Find the red blood cells and label each as P. falciparum-infected, uninfected, or of indeterminate infection status.
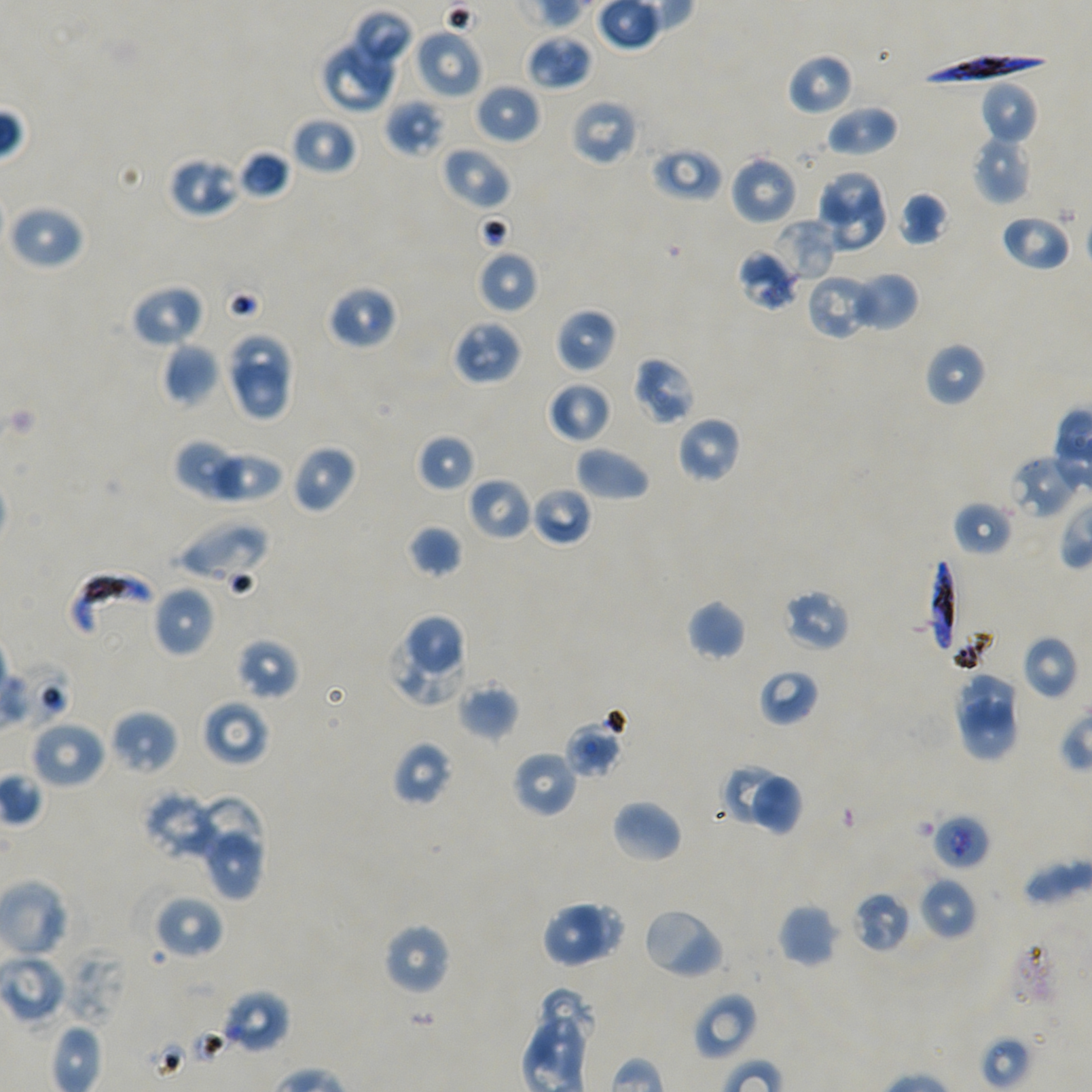
Approximate bounding rectangles given as corner coordinates in pixels from the top-left. Not every red blood cell is marked.
Infected red blood cells: (x1=921, y1=52, x2=1053, y2=88), (x1=928, y1=556, x2=960, y2=657), (x1=69, y1=570, x2=154, y2=640).
Red blood cells of indeterminate infection status: (x1=738, y1=249, x2=798, y2=311), (x1=175, y1=518, x2=268, y2=583), (x1=564, y1=718, x2=625, y2=779), (x1=930, y1=814, x2=989, y2=871).
Uninfected red blood cells: (x1=350, y1=10, x2=415, y2=75), (x1=412, y1=29, x2=483, y2=100), (x1=319, y1=35, x2=401, y2=112), (x1=526, y1=35, x2=592, y2=90), (x1=787, y1=52, x2=854, y2=116), (x1=980, y1=81, x2=1038, y2=145), (x1=475, y1=83, x2=541, y2=145), (x1=384, y1=97, x2=445, y2=158), (x1=570, y1=98, x2=640, y2=167), (x1=825, y1=103, x2=898, y2=158), (x1=290, y1=115, x2=357, y2=176), (x1=971, y1=132, x2=1033, y2=205), (x1=440, y1=145, x2=510, y2=210), (x1=649, y1=145, x2=723, y2=202), (x1=237, y1=150, x2=291, y2=200), (x1=729, y1=153, x2=798, y2=225), (x1=168, y1=156, x2=242, y2=217), (x1=815, y1=169, x2=886, y2=228), (x1=817, y1=192, x2=887, y2=256), (x1=898, y1=192, x2=949, y2=247), (x1=8, y1=203, x2=85, y2=271), (x1=1000, y1=213, x2=1072, y2=272), (x1=770, y1=219, x2=836, y2=285), (x1=475, y1=250, x2=539, y2=314), (x1=853, y1=271, x2=919, y2=331), (x1=807, y1=274, x2=878, y2=340), (x1=131, y1=285, x2=204, y2=347), (x1=327, y1=285, x2=398, y2=349), (x1=556, y1=308, x2=617, y2=374), (x1=451, y1=318, x2=524, y2=386), (x1=225, y1=334, x2=298, y2=396), (x1=163, y1=342, x2=221, y2=407), (x1=925, y1=342, x2=987, y2=406), (x1=632, y1=355, x2=697, y2=425), (x1=225, y1=363, x2=294, y2=422), (x1=547, y1=381, x2=613, y2=443), (x1=676, y1=416, x2=742, y2=484), (x1=416, y1=433, x2=477, y2=493), (x1=174, y1=439, x2=246, y2=500), (x1=291, y1=443, x2=356, y2=513), (x1=575, y1=445, x2=651, y2=501), (x1=201, y1=448, x2=285, y2=504), (x1=1006, y1=455, x2=1080, y2=520), (x1=467, y1=476, x2=532, y2=541), (x1=532, y1=486, x2=592, y2=547), (x1=952, y1=500, x2=1013, y2=558), (x1=407, y1=524, x2=464, y2=578), (x1=153, y1=585, x2=215, y2=657), (x1=780, y1=588, x2=851, y2=652), (x1=686, y1=599, x2=746, y2=661), (x1=387, y1=614, x2=469, y2=706), (x1=1021, y1=634, x2=1078, y2=700), (x1=236, y1=638, x2=300, y2=700), (x1=757, y1=668, x2=819, y2=727), (x1=953, y1=672, x2=1022, y2=729), (x1=456, y1=680, x2=519, y2=742), (x1=202, y1=700, x2=270, y2=766), (x1=958, y1=703, x2=1018, y2=761), (x1=109, y1=710, x2=179, y2=774), (x1=29, y1=718, x2=106, y2=790), (x1=393, y1=741, x2=455, y2=806), (x1=511, y1=750, x2=577, y2=817), (x1=719, y1=763, x2=782, y2=826), (x1=752, y1=771, x2=806, y2=840), (x1=143, y1=790, x2=219, y2=862), (x1=189, y1=790, x2=268, y2=873), (x1=611, y1=799, x2=683, y2=864), (x1=205, y1=828, x2=267, y2=904), (x1=919, y1=876, x2=978, y2=940), (x1=851, y1=890, x2=912, y2=953), (x1=153, y1=894, x2=225, y2=960), (x1=541, y1=899, x2=606, y2=968), (x1=778, y1=903, x2=838, y2=968), (x1=572, y1=904, x2=629, y2=959), (x1=641, y1=905, x2=727, y2=981), (x1=382, y1=922, x2=452, y2=996), (x1=0, y1=953, x2=66, y2=1025), (x1=534, y1=986, x2=592, y2=1066), (x1=220, y1=989, x2=291, y2=1055), (x1=691, y1=992, x2=758, y2=1061).

Thin blood film. Image is 1092×1092 pixels. Oil immersion, 100x objective (numerical aperture 1.45). Giemsa stain. P. falciparum strain NF54 maintained in static in-vitro culture. Donor blood group A+/O+. One field from this slide.